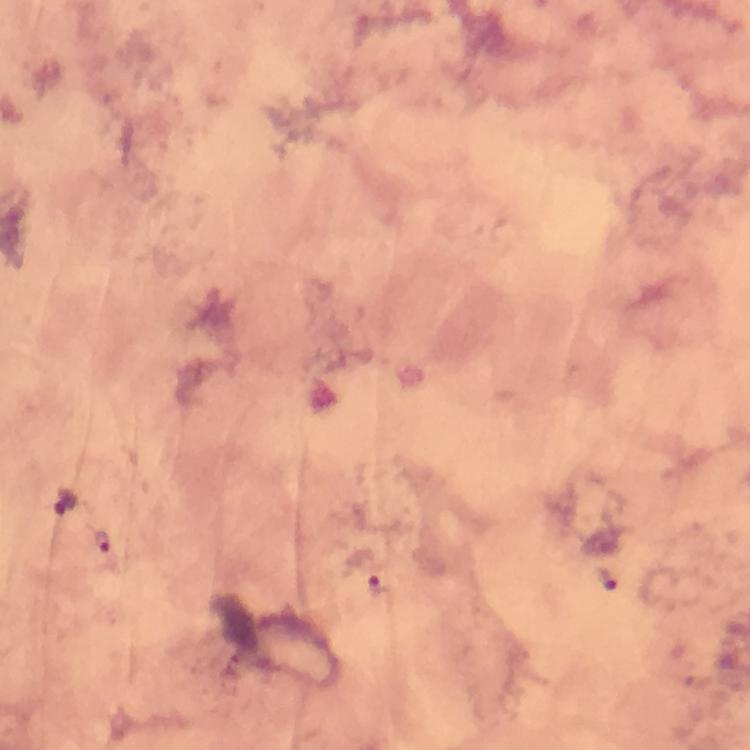

Approximate centers as [x, y] in pixels.
Summary:
  - Malaria parasite locations: [65, 498], [103, 541], [605, 577], [376, 584]
  - Cropped from: a single field of view
  - Immersion oil: used
  - Preparation: thick blood smear
  - Magnification: 100x
  - Image size: 750×750 pixels
  - Context: from a diagnostic examination for malaria
  - Capture: smartphone mounted on the microscope
  - Stain: Giemsa